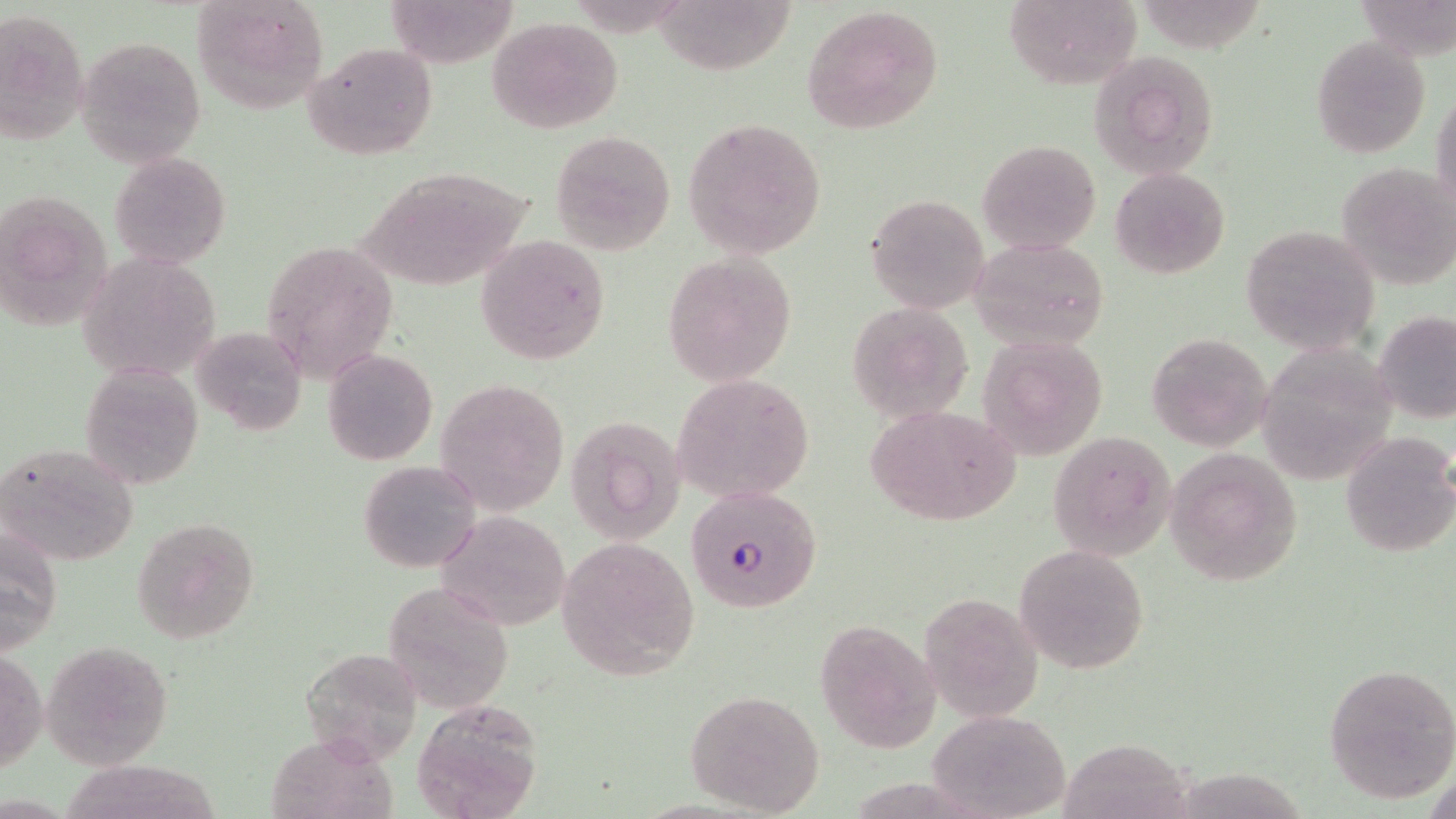

{
  "slide_level_diagnosis": "Plasmodium falciparum",
  "preparation": "thin blood film",
  "field_of_view": "one of a larger specimen",
  "uninfected_red_blood_cell_locations": "approximate bounding boxes as (x1, y1, x2, y2) in pixels: (190, 0, 330, 116), (382, 0, 520, 67), (1001, 0, 1142, 89), (1354, 0, 1454, 60), (656, 1, 795, 75), (800, 4, 946, 138), (0, 10, 89, 143), (488, 15, 623, 133), (74, 36, 206, 167), (1310, 36, 1430, 156), (304, 42, 438, 159), (1087, 50, 1219, 180), (1431, 85, 1456, 223), (684, 117, 827, 258), (550, 130, 676, 255), (977, 138, 1101, 253), (109, 150, 231, 270), (1335, 161, 1456, 289), (355, 165, 533, 292), (1108, 166, 1231, 280), (0, 188, 115, 332), (866, 193, 991, 314), (1240, 224, 1382, 356), (474, 234, 613, 367), (971, 237, 1109, 349), (260, 240, 399, 383), (80, 252, 222, 384), (662, 253, 799, 385), (847, 299, 974, 423), (1373, 310, 1455, 424), (191, 325, 306, 435), (1145, 331, 1274, 454), (976, 333, 1108, 459), (1252, 342, 1397, 481), (323, 348, 437, 464), (77, 363, 203, 489), (672, 372, 815, 503), (435, 378, 570, 516), (864, 404, 1023, 527), (566, 417, 687, 545), (1339, 429, 1456, 559), (1047, 431, 1175, 560), (1, 444, 140, 568), (1164, 449, 1302, 585), (358, 458, 482, 573), (434, 510, 569, 629), (131, 515, 259, 643), (1, 523, 64, 653), (557, 536, 702, 679), (1013, 543, 1150, 674), (382, 578, 514, 714), (925, 594, 1054, 731), (814, 618, 941, 751), (43, 641, 174, 770), (298, 645, 424, 768), (1, 646, 45, 774), (1323, 664, 1456, 802), (683, 688, 824, 816), (418, 700, 551, 816), (926, 708, 1070, 817), (256, 727, 405, 816), (1066, 732, 1203, 819), (60, 756, 235, 819), (1172, 757, 1307, 816)",
  "stain": "May-Grünwald-Giemsa",
  "plasmodium_falciparum_infected_red_blood_cell_locations": "approximate bounding boxes as (x1, y1, x2, y2) in pixels: (683, 485, 821, 612)",
  "magnification": "1000x",
  "image_size": "1456×819 pixels",
  "modality": "optical microscopy"
}